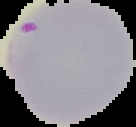

From a thin blood smear. Image is 136×127 pixels. The area outside the segmented cell region is set to black. Malaria status: parasitized.